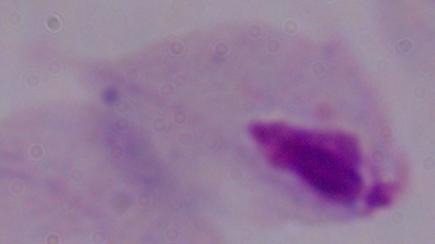

magnification = 1000x
identification = trichomonad
modality = micrograph